Locate every Plasmodium parasite.
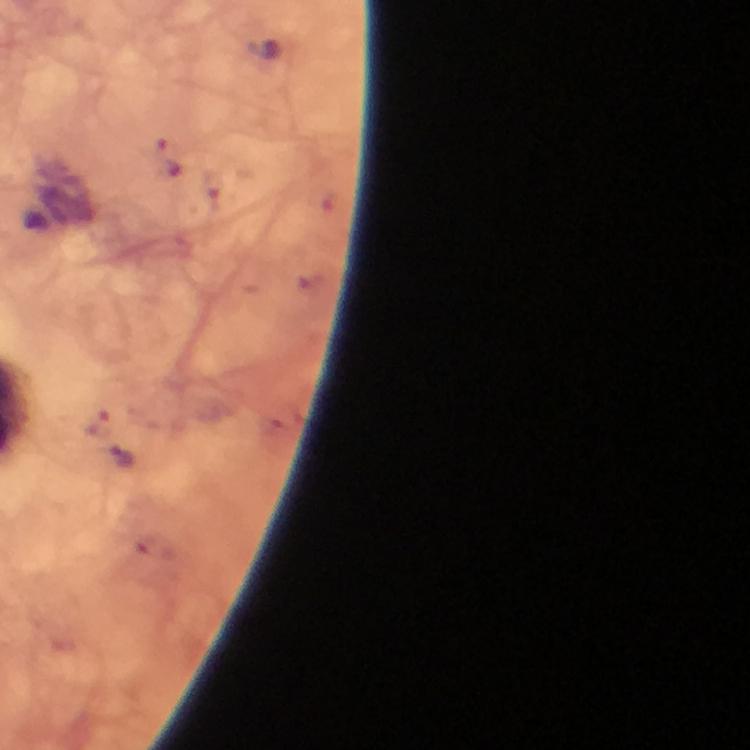

Approximate centers as [x, y] in pixels.
Plasmodium parasites: [122, 456].

context = from a diagnostic examination for malaria
image size = 750×750 pixels
stain = Giemsa
preparation = thick blood film
immersion oil = used
capture = smartphone mounted on the microscope
cropped from = one field of view
magnification = 100x